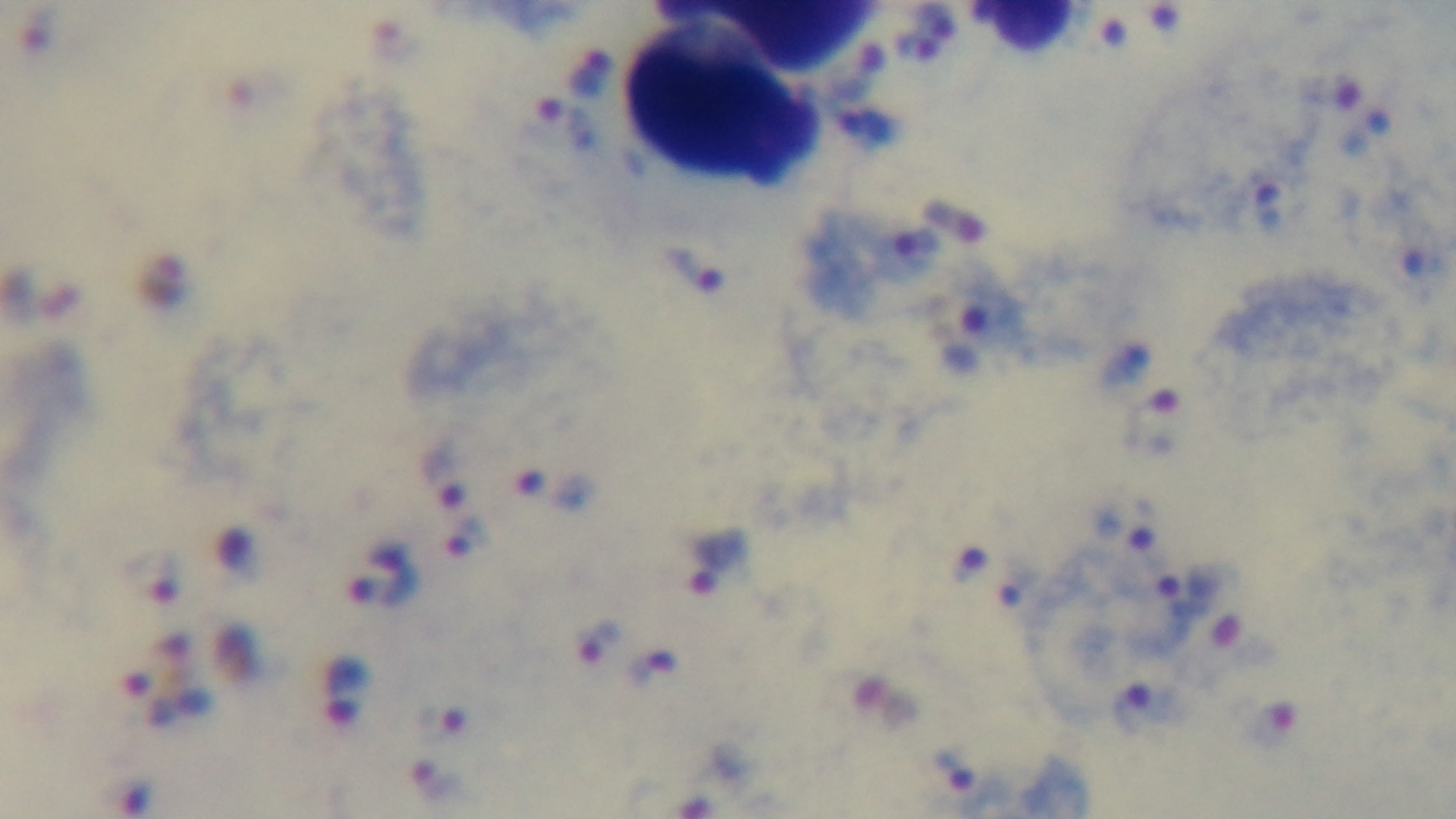

Single field of view. 100x oil-immersion objective. Giemsa stain. Preparation: thick blood film. Malaria status: positive. Mounted 4K digital camera. Light microscopy.